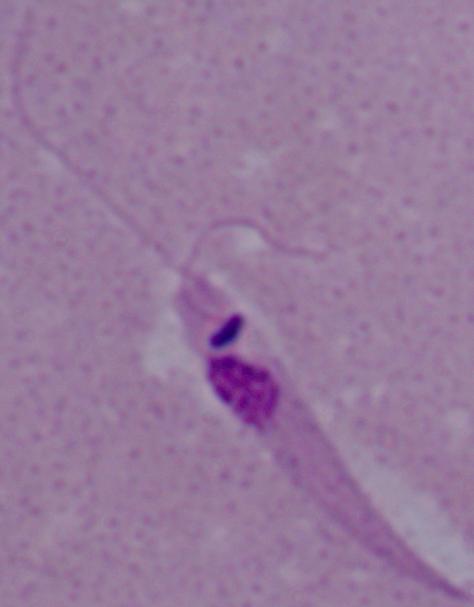

modality: photomicrograph
magnification: 1000x
identification: Leishmania